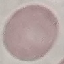 Malaria status: uninfected. Photographed with a smartphone camera at the microscope eyepiece. Giemsa stain. Thin blood film. Cell patch, automatically extracted from a larger field of view and resized to 64 × 64 pixels.